Assess for Plasmodium parasites.
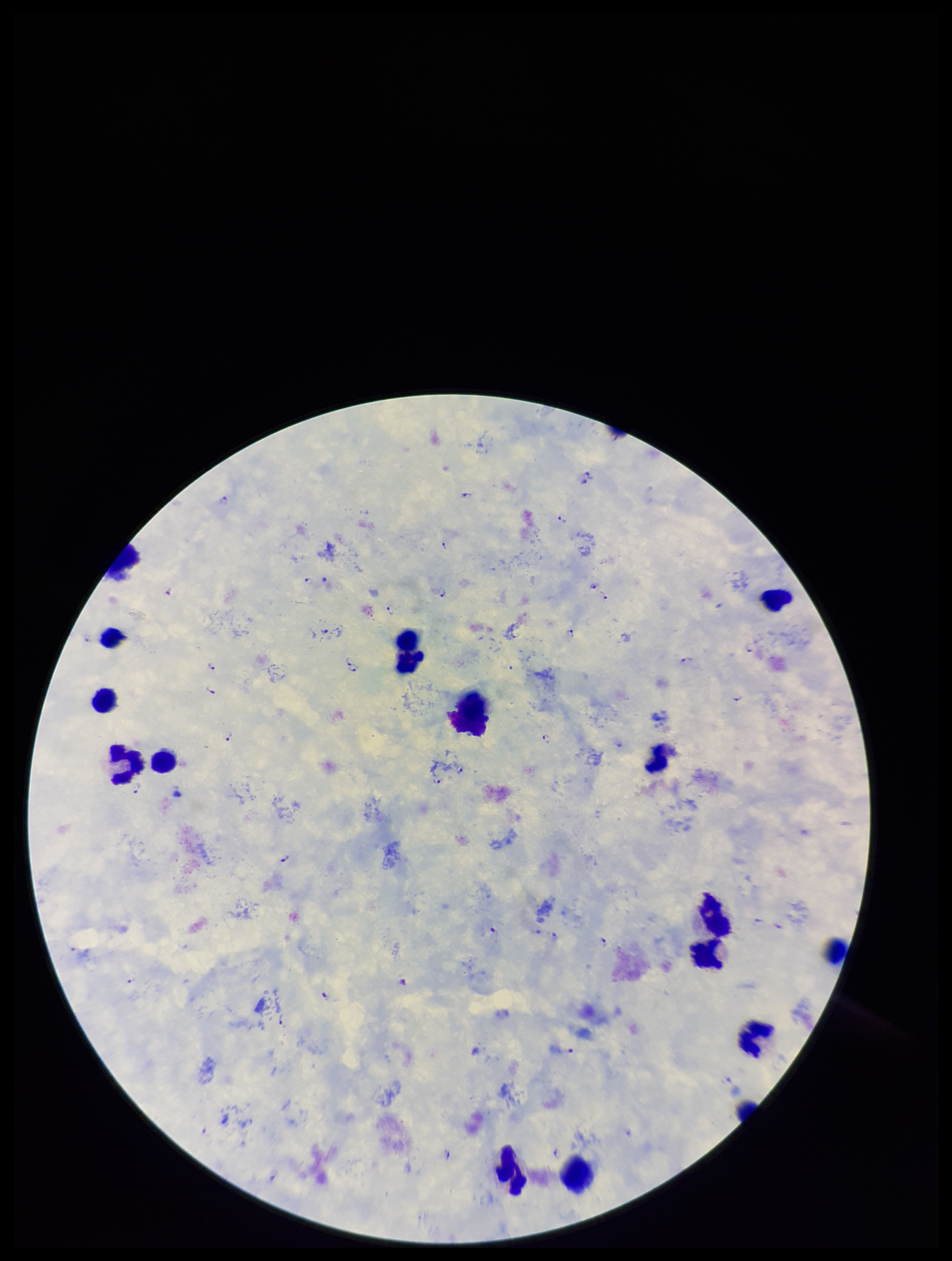
Detected.

species reported for this patient = Plasmodium falciparum
field of view = one from this slide
stain = Giemsa
patient malaria status = positive
preparation = thick blood smear
image size = 952×1261 pixels
leukocyte count = 15
capture = smartphone photograph through the microscope eyepiece
parasite count = 35